Report the malaria status.
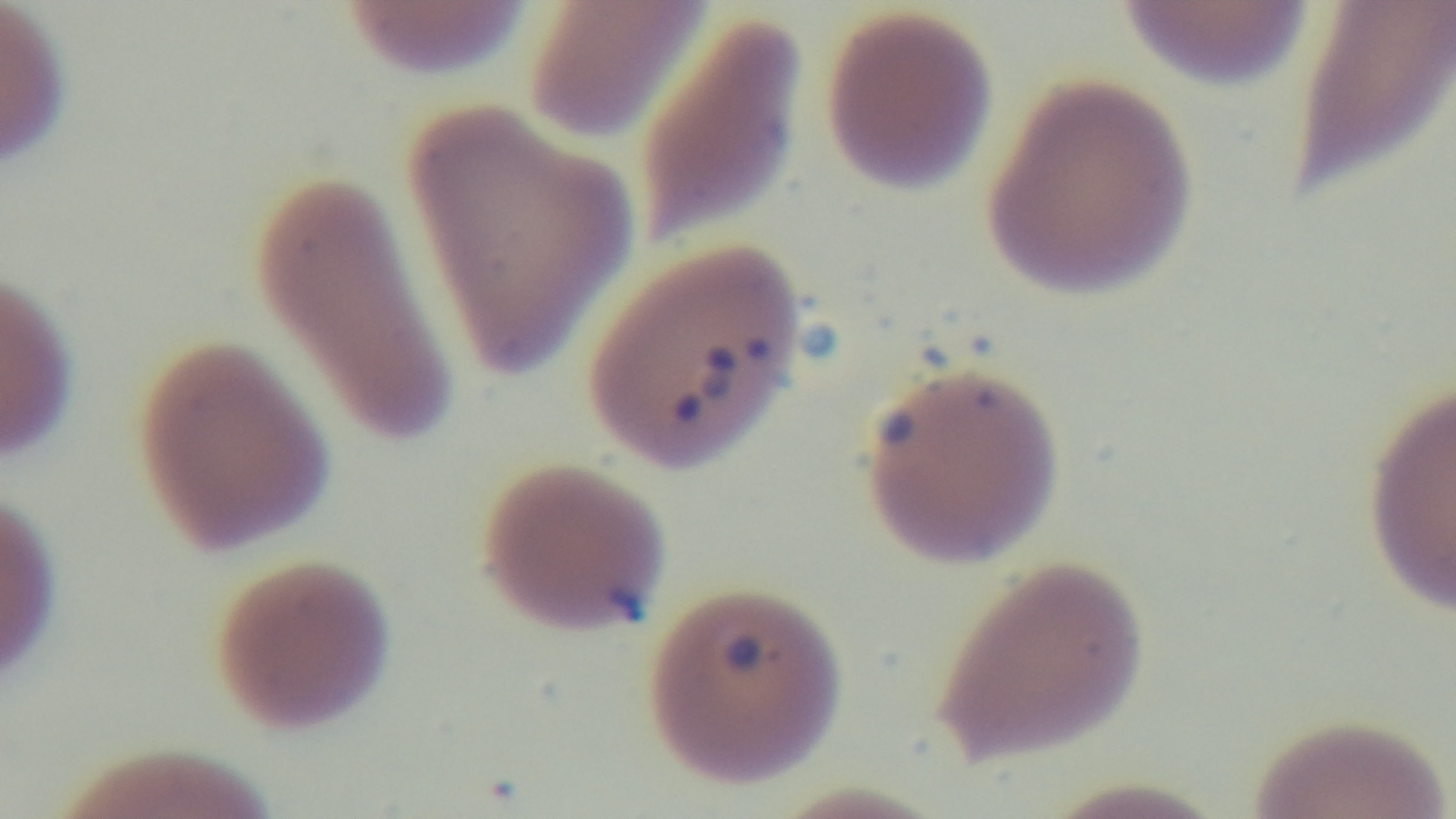
Infected.

{
  "preparation": "thin smear",
  "stain": "Giemsa",
  "objective": "100x oil immersion",
  "field_of_view": "one from the slide",
  "modality": "light microscopy",
  "capture": "mounted 4K digital camera"
}